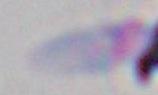

Micrograph. 1000x magnification. Toxoplasma gondii is shown.